Outline each white blood cell.
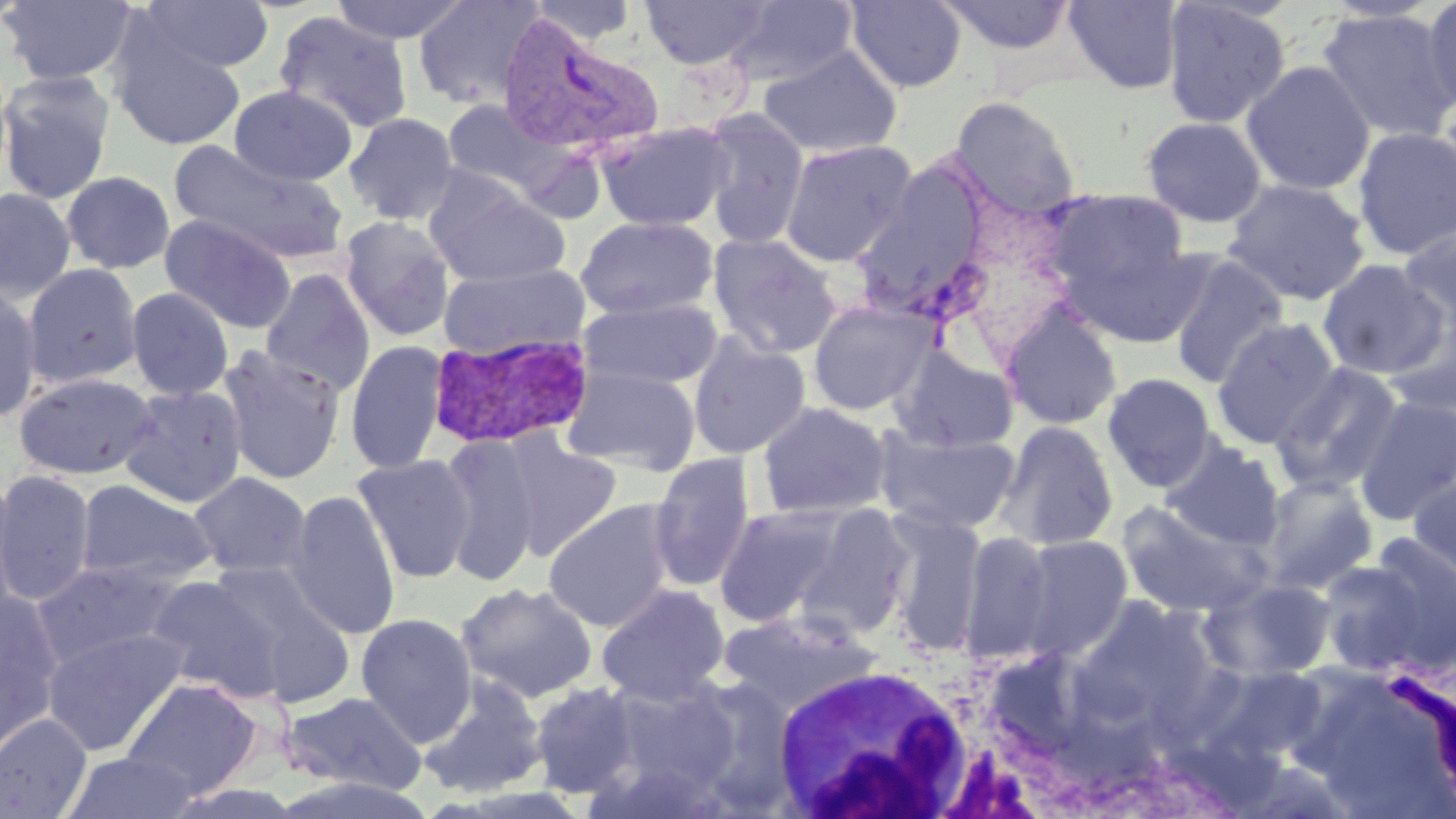
Approximate bounding boxes as (x1,y1)-(x2,y2) corner pairs in pixels.
White blood cells: (767,662)-(978,816).

Plasmodium vivax-infected red blood cell locations: (496,13)-(664,160), (427,331)-(595,450). Uninfected red blood cell locations: (1,0)-(137,87), (329,0)-(471,45), (412,0)-(546,110), (527,0)-(639,46), (640,0)-(770,69), (726,0)-(858,87), (935,0)-(1079,56), (1062,0)-(1185,94), (138,1)-(274,73), (844,1)-(967,93), (1160,1)-(1291,129), (1420,1)-(1456,116), (1317,8)-(1456,143), (274,11)-(413,134), (108,24)-(247,151), (758,44)-(902,159), (1241,60)-(1376,196), (0,71)-(116,204), (229,86)-(357,186), (950,95)-(1082,217), (439,99)-(567,200), (699,109)-(810,249), (344,112)-(460,225), (1141,116)-(1267,228), (595,121)-(735,232), (1352,126)-(1456,260), (779,139)-(917,266), (168,141)-(348,264), (61,171)-(175,274), (852,171)-(993,317), (424,176)-(570,288), (1223,178)-(1370,306), (0,187)-(76,302), (1045,188)-(1192,306), (159,214)-(297,334), (338,215)-(456,342), (576,216)-(719,319), (1396,223)-(1456,338), (707,233)-(842,359), (1168,252)-(1288,389), (1317,260)-(1450,379), (22,263)-(144,390), (438,263)-(589,360), (259,268)-(375,396), (0,284)-(43,422), (126,287)-(234,401), (579,297)-(723,390), (807,300)-(938,415), (1000,304)-(1123,430), (1384,312)-(1456,417), (1211,317)-(1341,450), (687,334)-(810,459), (345,340)-(449,474), (217,345)-(347,485), (890,347)-(1018,452), (1270,362)-(1404,495), (560,365)-(702,474), (14,372)-(159,479), (1102,373)-(1218,492), (119,384)-(247,508), (1354,395)-(1456,526), (756,401)-(891,519), (996,421)-(1119,550), (873,427)-(1020,534), (437,432)-(541,586), (499,433)-(623,560), (1162,442)-(1284,549), (351,453)-(477,584), (648,453)-(756,593), (0,470)-(96,607), (1408,470)-(1456,582), (188,471)-(313,580), (0,472)-(22,620), (1259,474)-(1377,593), (74,479)-(218,589), (285,489)-(402,640), (543,499)-(678,632), (1117,500)-(1271,618), (713,504)-(849,627), (794,505)-(915,636), (884,512)-(987,652), (960,530)-(1054,661), (1017,535)-(1133,657), (1317,554)-(1450,677), (30,559)-(187,670), (206,559)-(357,706), (144,576)-(287,701), (1201,577)-(1338,682), (457,582)-(598,703), (596,583)-(731,705), (1,591)-(65,755), (1068,597)-(1219,734), (718,609)-(878,715), (356,613)-(478,746), (41,626)-(190,757), (1200,661)-(1332,766), (1376,665)-(1456,810), (418,673)-(550,799), (677,675)-(801,816), (118,676)-(265,800), (598,677)-(742,807), (528,681)-(642,798), (279,690)-(428,796), (0,713)-(92,819), (64,750)-(201,818). Slide-level diagnosis: Plasmodium vivax. Image is 1456×819 pixels. Light microscopy. Thin blood film. 1000x magnification. May-Grünwald-Giemsa stain. One field of a larger specimen.